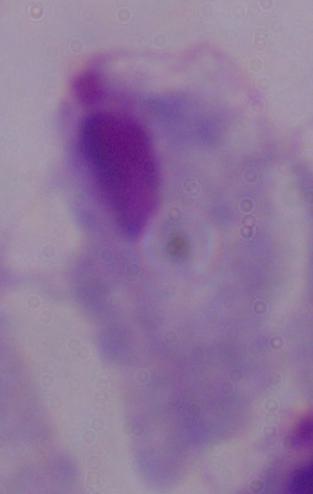
{
  "magnification": "1000x",
  "modality": "photomicrograph",
  "identification": "trichomonad"
}